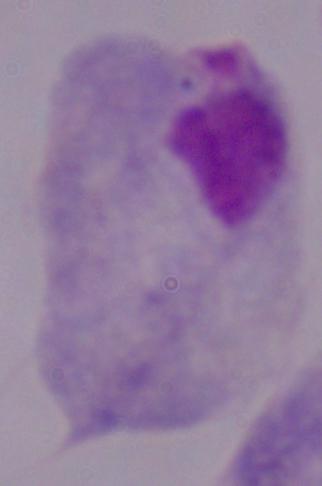

Summary:
  - Identification: trichomonad
  - Magnification: 1000x
  - Modality: micrograph